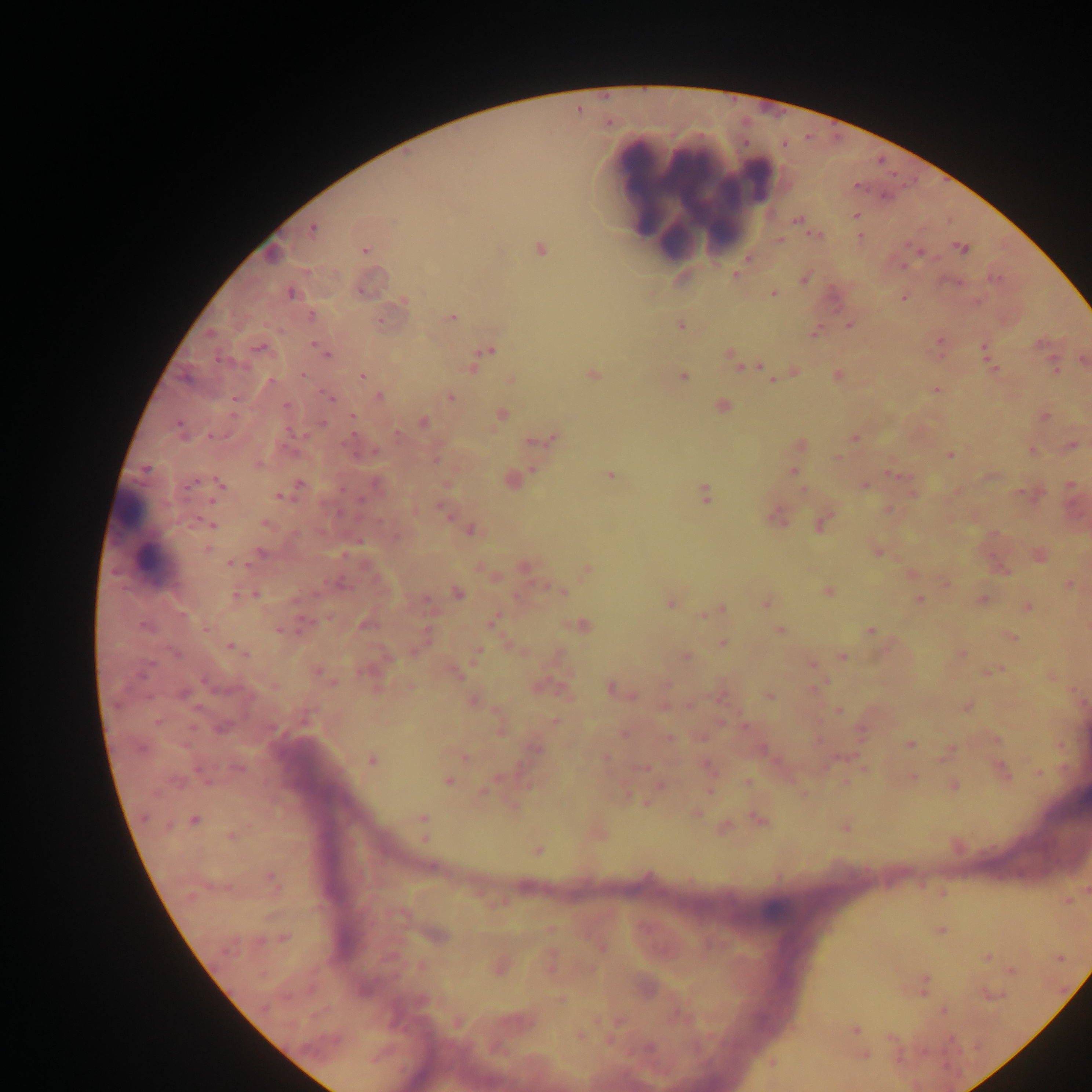

capture = mobile-phone photograph through a microscope
Plasmodium parasite locations = approximate centers as (x, y) in pixels: (855, 186), (855, 216), (797, 219), (313, 229), (816, 236), (860, 237), (780, 240), (540, 249), (961, 249), (365, 250), (919, 251), (902, 267), (735, 275), (804, 279), (361, 292), (290, 293), (772, 294), (903, 298), (403, 301), (311, 316), (452, 317), (380, 322), (849, 325), (681, 326), (814, 333), (210, 334), (939, 340), (314, 344), (258, 348), (983, 348), (488, 351), (327, 353), (730, 356), (219, 360), (739, 364), (757, 366), (472, 368), (994, 368), (1055, 368), (592, 374), (302, 375), (362, 376), (683, 376), (837, 376), (771, 379), (270, 381), (936, 389), (380, 396), (450, 397), (330, 398), (286, 405), (721, 406), (501, 414), (1045, 416), (352, 417), (423, 421), (322, 424), (178, 425), (213, 436), (855, 437), (554, 438), (543, 440), (348, 442), (532, 442), (801, 444), (1072, 445), (1032, 450), (374, 452), (949, 455), (838, 459), (258, 464), (146, 469), (793, 472), (895, 475), (610, 476), (797, 476), (512, 480), (219, 483), (300, 484), (864, 485), (1070, 485), (803, 491), (705, 493), (279, 497), (361, 498), (444, 510), (776, 517), (210, 524), (265, 524), (822, 524), (470, 530), (207, 549), (261, 552), (878, 552), (232, 564), (525, 567), (587, 570), (911, 574), (1070, 584), (561, 592), (829, 592), (457, 593), (237, 594), (256, 594), (982, 599), (919, 600), (426, 601), (670, 603), (767, 603), (1027, 607), (722, 609), (184, 614), (703, 614), (492, 621), (365, 625), (583, 625), (145, 627), (206, 628), (278, 629), (870, 630), (780, 631), (1012, 638), (722, 643), (231, 647), (478, 652), (175, 653), (961, 655), (685, 657), (843, 657), (812, 664), (318, 672), (990, 672), (142, 673), (456, 674), (814, 688), (610, 689), (184, 694), (769, 696), (472, 701), (966, 707), (839, 711), (156, 722), (554, 722), (224, 727), (500, 728), (623, 734), (669, 738), (996, 739), (909, 744), (140, 749), (536, 750), (464, 756), (606, 758), (372, 760), (707, 765), (642, 767), (238, 769), (1003, 770), (1040, 772), (913, 778), (448, 781), (747, 782), (954, 785), (659, 786), (484, 791), (697, 813), (143, 818), (422, 818), (759, 819), (194, 820), (845, 827), (231, 836), (424, 837), (537, 851), (272, 881), (941, 930), (284, 938), (261, 941), (602, 947), (986, 957), (1012, 970), (924, 984), (943, 1010), (855, 1030), (580, 1036), (649, 1048), (924, 1052), (865, 1055)
field of view = single
image size = 1092×1092 pixels
country = Ghana
preparation = thick blood film
leukocyte locations = approximate centers as (x, y) in pixels: (648, 188), (694, 191), (140, 532)